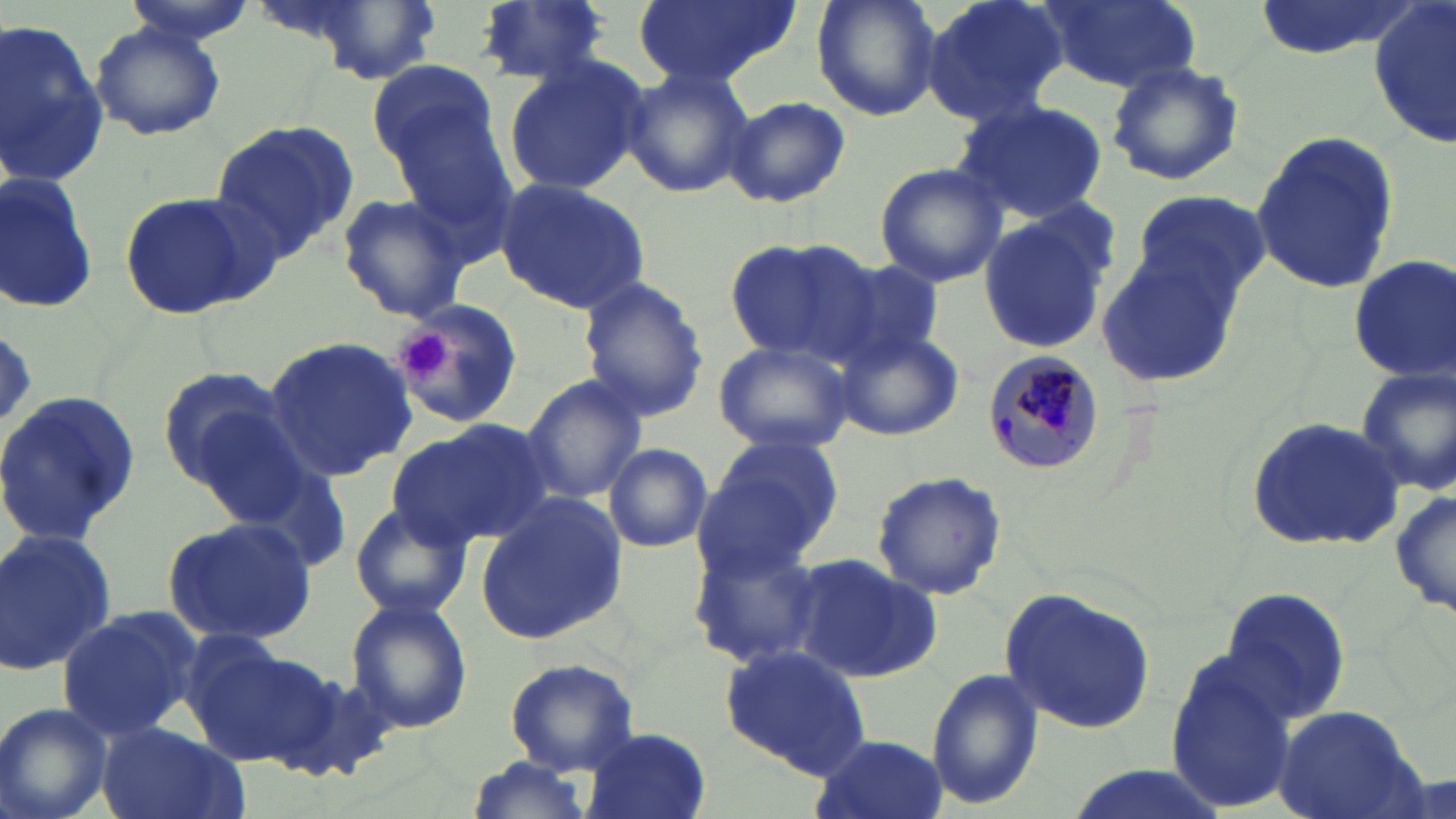
Plasmodium malariae-infected red blood cell locations = approximate bounding boxes as [x1, y1, x2, y2] in pixels: [981, 351, 1104, 478]
slide-level diagnosis = Plasmodium malariae
preparation = thin blood film
modality = optical microscopy
platelet locations = approximate bounding boxes as [x1, y1, x2, y2] in pixels: [401, 333, 448, 382]
magnification = 1000x
uninfected red blood cell locations = approximate bounding boxes as [x1, y1, x2, y2] in pixels: [121, 0, 263, 50], [473, 0, 613, 87], [633, 0, 796, 87], [810, 0, 943, 122], [918, 0, 1068, 128], [1040, 0, 1200, 93], [1246, 0, 1420, 60], [1370, 3, 1455, 150], [0, 21, 109, 187], [89, 22, 225, 141], [502, 56, 647, 196], [367, 59, 499, 167], [1104, 59, 1245, 187], [620, 66, 752, 199], [386, 77, 516, 246], [726, 97, 850, 209], [951, 98, 1109, 223], [210, 120, 361, 254], [1249, 131, 1400, 296], [873, 163, 1007, 287], [0, 171, 101, 317], [493, 178, 652, 314], [1131, 188, 1271, 307], [118, 191, 270, 321], [333, 191, 472, 323], [980, 217, 1109, 353], [722, 239, 883, 364], [1097, 252, 1243, 389], [1348, 256, 1456, 385], [828, 259, 949, 368], [578, 276, 710, 424], [391, 300, 525, 430], [835, 327, 965, 442], [262, 335, 416, 479], [712, 338, 856, 456], [1353, 365, 1456, 497], [156, 366, 302, 492], [519, 374, 648, 503], [0, 391, 144, 549], [387, 418, 555, 554], [1243, 418, 1407, 551], [701, 434, 846, 568], [604, 442, 713, 553], [869, 469, 1007, 601], [1390, 487, 1455, 619], [473, 494, 626, 645], [347, 504, 472, 623], [161, 513, 318, 648], [0, 528, 117, 679], [687, 539, 828, 667], [792, 553, 940, 683], [1220, 585, 1353, 724], [1001, 587, 1156, 734], [345, 596, 474, 735], [55, 604, 203, 741], [178, 636, 336, 772], [720, 644, 871, 775], [1163, 650, 1296, 813], [503, 657, 641, 774], [926, 668, 1043, 811], [0, 703, 115, 819], [1274, 704, 1421, 819], [96, 723, 245, 819], [581, 728, 712, 819], [808, 731, 948, 819], [459, 756, 598, 819], [1055, 765, 1237, 819]
stain = May-Grünwald-Giemsa
image size = 1456×819 pixels
field of view = one of a larger specimen